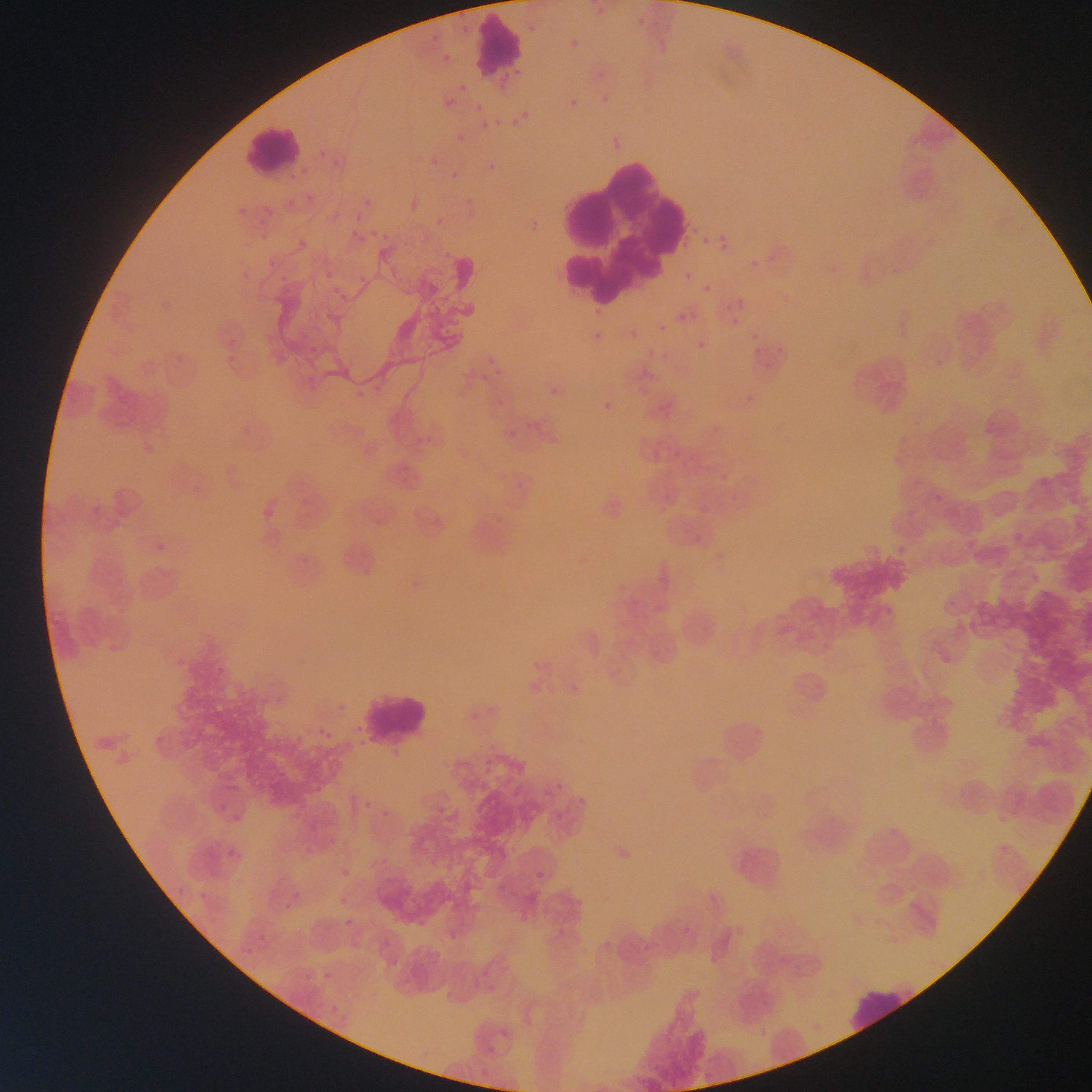
{
  "leukocyte_locations": "approximate bounding boxes as {left, top, right, bottom} in pixels: {471, 14, 525, 79}, {240, 122, 306, 175}, {557, 141, 682, 310}, {354, 689, 434, 748}, {846, 988, 915, 1031}",
  "preparation": "thin blood film",
  "field_of_view": "single",
  "country": "Ghana",
  "plasmodium_parasite_locations": "approximate bounding boxes as {left, top, right, bottom} in pixels: {525, 18, 547, 36}, {564, 35, 582, 56}, {435, 43, 459, 65}, {435, 79, 465, 111}, {559, 83, 588, 108}, {596, 85, 615, 113}, {469, 91, 494, 114}, {508, 95, 537, 123}, {483, 105, 516, 129}, {446, 126, 473, 142}, {320, 147, 328, 154}, {330, 148, 354, 173}, {484, 150, 500, 172}, {421, 156, 440, 171}, {444, 166, 463, 187}, {303, 190, 314, 206}, {462, 195, 475, 206}, {263, 197, 279, 214}, {359, 197, 370, 211}, {234, 205, 241, 214}, {355, 220, 377, 244}, {293, 222, 329, 247}, {248, 224, 264, 239}, {702, 238, 710, 245}, {721, 244, 729, 253}, {262, 250, 287, 268}, {359, 258, 384, 285}, {273, 269, 301, 297}, {683, 272, 692, 282}, {322, 274, 338, 294}, {703, 284, 711, 293}, {737, 298, 746, 308}, {675, 312, 684, 321}, {299, 319, 317, 332}, {586, 322, 608, 341}, {658, 323, 667, 332}, {626, 324, 643, 340}, {750, 332, 758, 340}, {697, 341, 706, 350}, {471, 351, 496, 381}, {933, 353, 947, 372}, {550, 371, 583, 397}, {506, 390, 557, 439}, {597, 396, 615, 410}, {984, 426, 991, 435}, {694, 468, 706, 481}, {708, 472, 727, 488}, {652, 503, 665, 516}, {154, 525, 177, 556}, {358, 559, 384, 580}, {409, 578, 422, 591}, {315, 719, 342, 744}, {481, 755, 496, 776}, {538, 776, 566, 808}, {359, 791, 372, 811}, {436, 800, 447, 818}, {216, 802, 231, 818}, {378, 808, 387, 826}, {556, 812, 572, 834}, {229, 815, 243, 827}, {223, 845, 240, 864}, {342, 862, 360, 881}, {529, 871, 540, 886}, {171, 884, 189, 900}, {334, 888, 354, 913}, {198, 890, 211, 908}, {282, 892, 304, 911}, {340, 910, 351, 929}, {250, 922, 279, 953}, {324, 970, 333, 981}, {300, 974, 311, 993}",
  "image_size": "1092×1092 pixels",
  "capture": "mobile-phone photograph through a microscope"
}